Assess this cell for malaria.
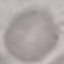

It is uninfected.

preparation = thin smear
capture = smartphone through the microscope eyepiece
stain = Giemsa
image type = cell patch, automatically extracted from a larger field of view and resized to 64 × 64 pixels